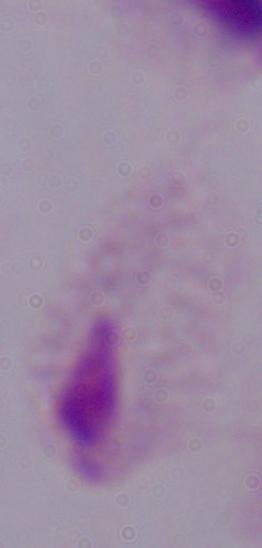
1000x magnification. A trichomonad is seen. Photomicrograph.